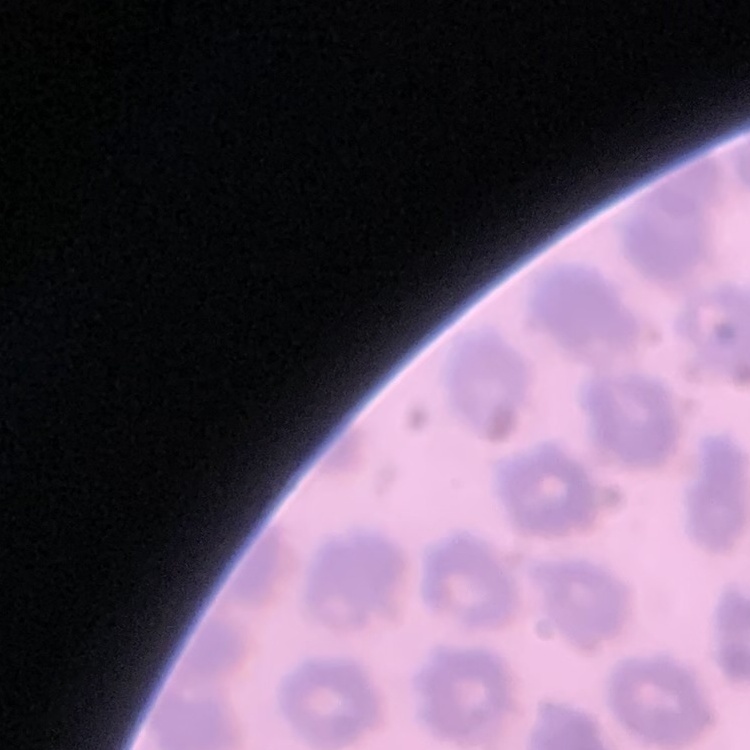 The erythrocytes show no rouleaux formation. Field's or Giemsa stain. Square crop of a larger photomicrograph. Thin peripheral smear.